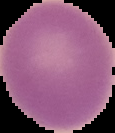
image_type: cell region segmented out of the field of view; surrounding area masked to black
image_size: 115×133 pixels
preparation: thin blood film
result: no Plasmodium parasites detected